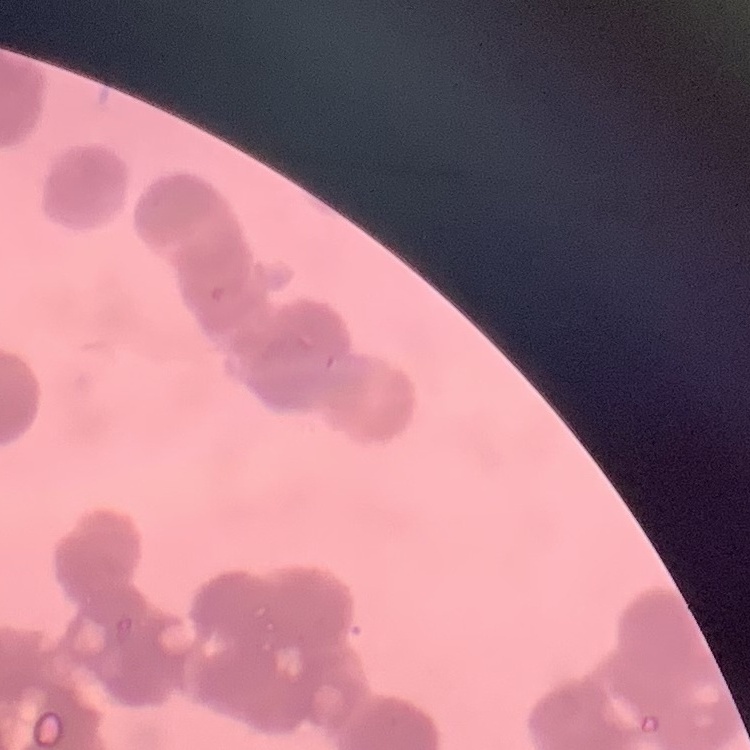

Summary:
  - Red blood cell morphology: rouleaux formation
  - Image type: square crop of a larger photomicrograph
  - Preparation: thin peripheral smear
  - Stain: Field's or Giemsa